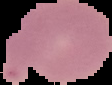
{
  "preparation": "thin blood smear",
  "image_type": "cell region segmented out of the field of view; surrounding area masked to black",
  "malaria_status": "uninfected",
  "image_size": "112×85 pixels"
}